Classify this cell by malaria status.
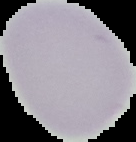
Uninfected.

Summary:
  - Preparation: thin blood smear
  - Image type: segmented cell region on a black background
  - Image size: 136×142 pixels